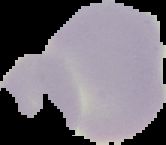
Image is 166×145 pixels. The area outside the segmented cell region is set to black. From a thin blood smear. Result: no malaria parasites detected.